Outline platelets.
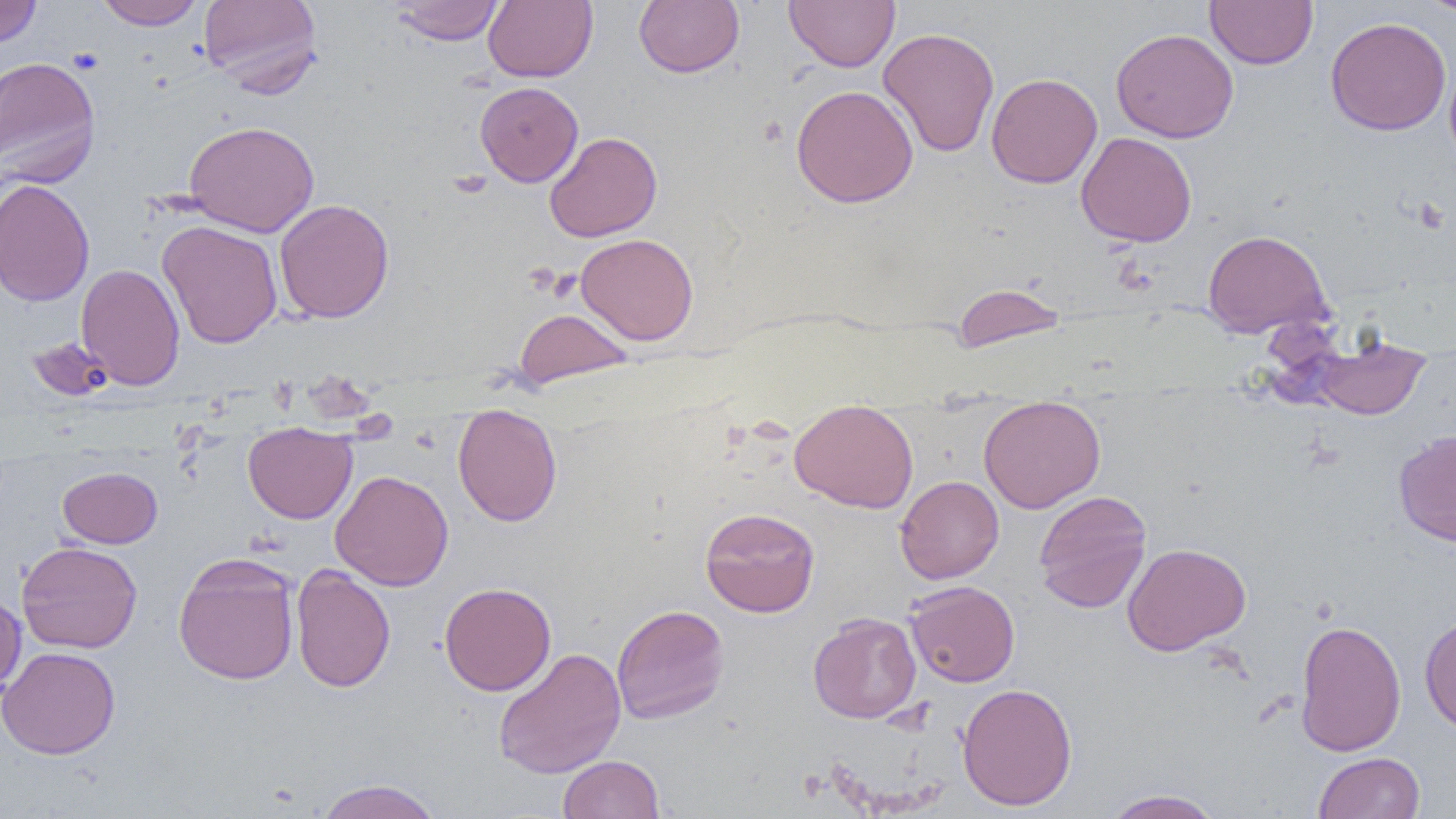

Approximate bounding boxes as (x1, y1, x2, y2) in pixels.
Platelets: (66, 48, 104, 74).

Summary:
  - Uninfected red blood cell locations: (0, 0, 42, 49), (94, 0, 205, 30), (198, 0, 322, 95), (634, 0, 744, 77), (784, 0, 900, 73), (1205, 0, 1318, 69), (1418, 0, 1456, 16), (389, 1, 505, 46), (483, 1, 598, 83), (1325, 17, 1451, 136), (878, 27, 999, 157), (1111, 28, 1239, 143), (1444, 55, 1456, 172), (0, 56, 101, 187), (987, 72, 1103, 189), (475, 81, 583, 187), (791, 85, 919, 208), (183, 120, 319, 236), (175, 121, 300, 352), (544, 131, 662, 242), (1076, 132, 1197, 247), (0, 178, 95, 307), (275, 199, 394, 323), (157, 220, 283, 349), (1202, 229, 1331, 338), (575, 232, 699, 345), (76, 262, 186, 391), (950, 282, 1070, 354), (514, 307, 634, 389), (1314, 334, 1430, 419), (978, 395, 1106, 514), (789, 398, 919, 514), (452, 406, 563, 527), (242, 423, 357, 524), (1393, 429, 1456, 547), (57, 467, 162, 548), (330, 469, 454, 591), (895, 475, 1004, 583), (1033, 490, 1152, 614), (699, 507, 820, 618), (16, 541, 143, 653), (1123, 542, 1251, 655), (173, 552, 301, 685), (291, 565, 396, 693), (905, 580, 1020, 687), (439, 582, 557, 696), (0, 588, 26, 697), (611, 603, 730, 724), (808, 612, 921, 723), (1419, 614, 1456, 733), (1295, 619, 1406, 756), (0, 646, 121, 759), (493, 647, 627, 779), (957, 682, 1077, 811), (1313, 752, 1425, 819), (558, 754, 664, 818), (313, 778, 444, 819), (1102, 788, 1225, 818)
  - Slide-level diagnosis: negative for blood parasites
  - Field of view: single
  - Modality: optical microscopy
  - Image size: 1456×819 pixels
  - Magnification: 1000x
  - Preparation: thin blood film